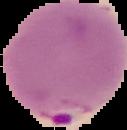
preparation = thin blood smear
image size = 127×130 pixels
image type = cell region segmented out of the field of view; surrounding area masked to black
result = Plasmodium parasites identified